Name the cell type shown.
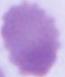

This is an erythrocyte.

magnification = 1000x
modality = micrograph